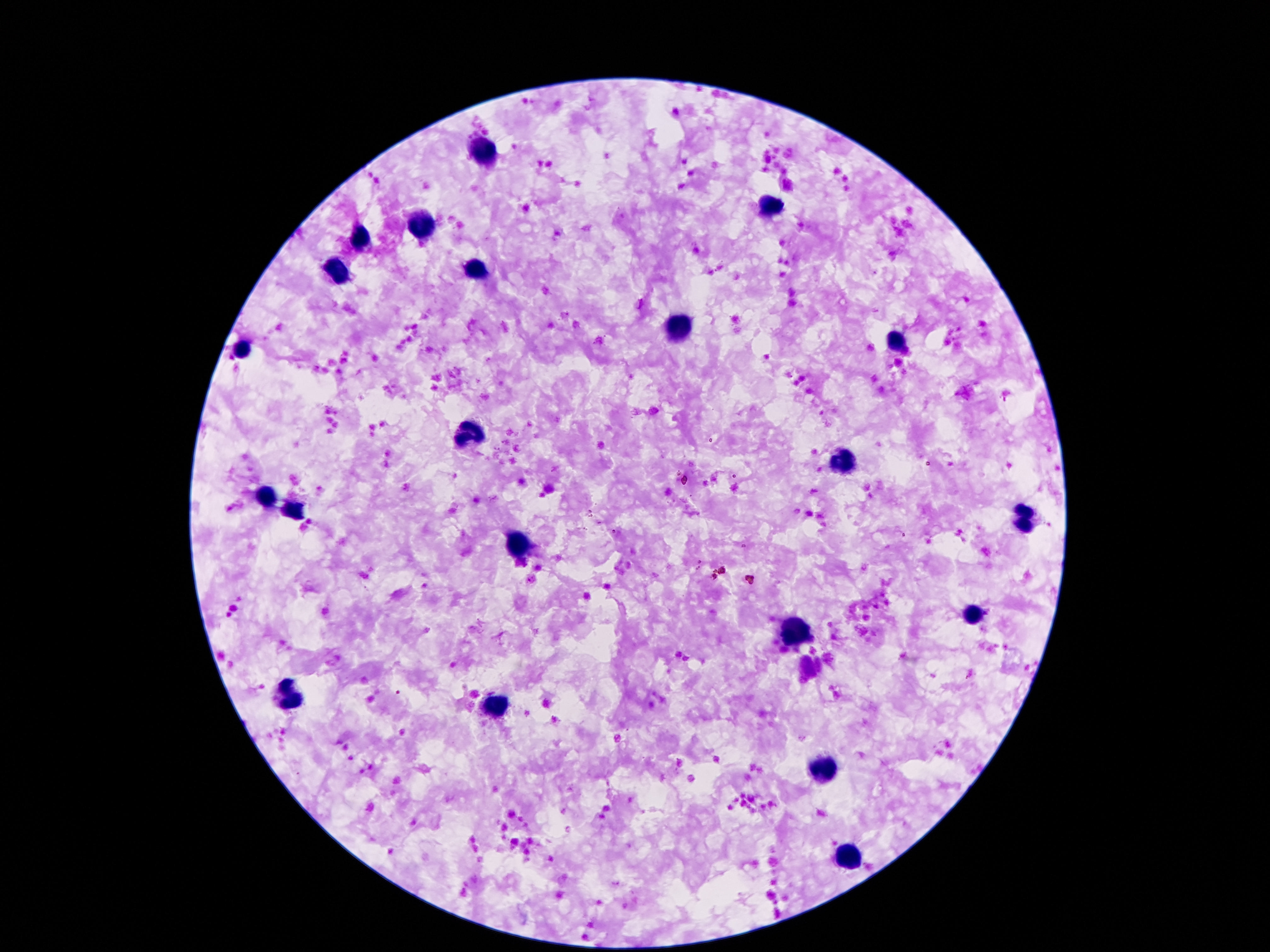
stain = Giemsa
image size = 1270×952 pixels
leukocyte locations = approximate object centers, in pixels from the top-left corner: (x=481, y=150), (x=770, y=209), (x=419, y=227), (x=360, y=236), (x=477, y=269), (x=337, y=271), (x=675, y=329), (x=895, y=343), (x=241, y=351), (x=468, y=432), (x=845, y=460), (x=264, y=496), (x=296, y=514), (x=1024, y=519), (x=516, y=545), (x=972, y=614), (x=796, y=636), (x=288, y=696), (x=495, y=706), (x=825, y=772), (x=850, y=860)
capture = smartphone camera through the microscope eyepiece
preparation = thick blood smear
patient malaria status = negative
field of view = single
magnification = 100x